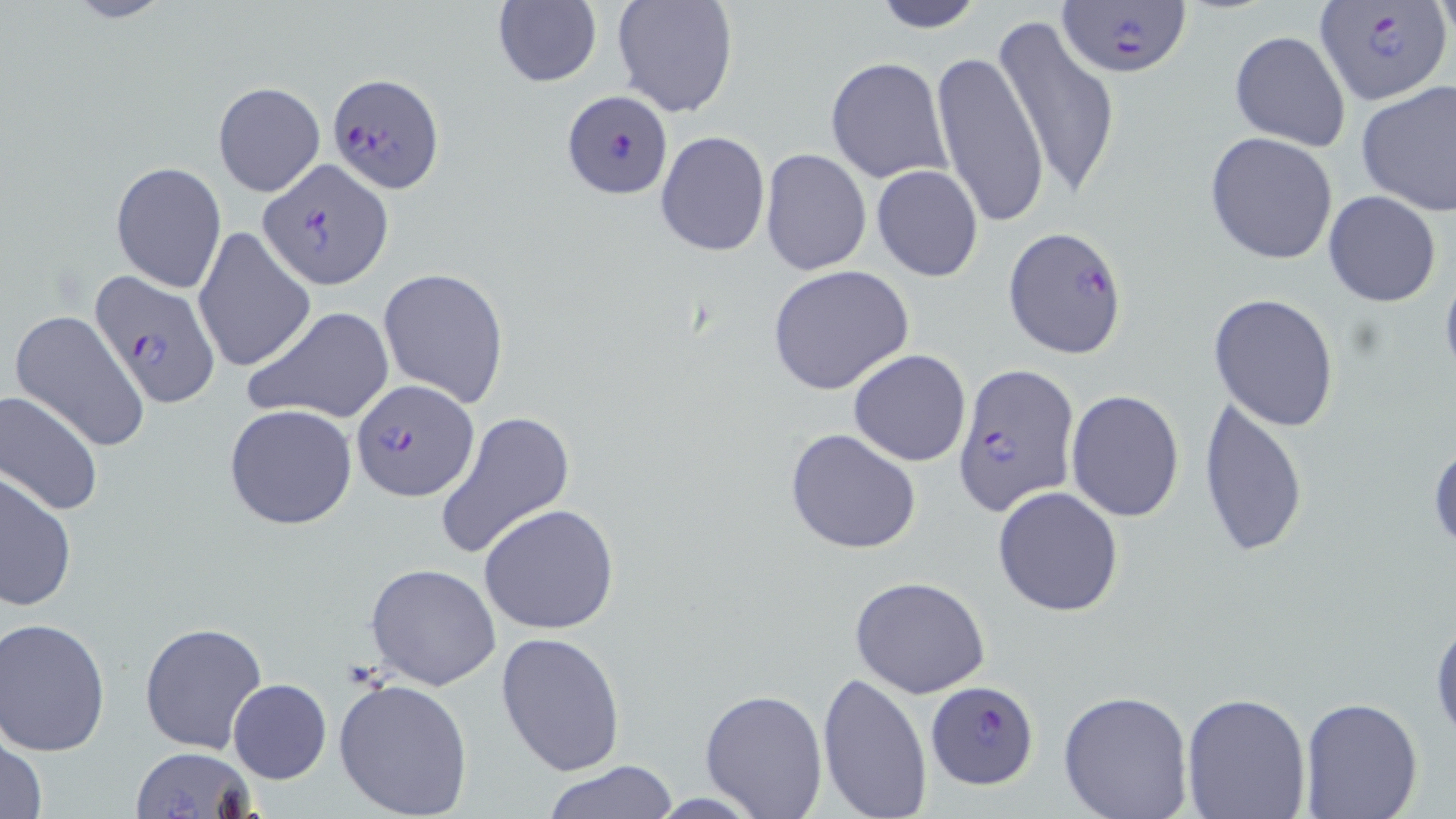

Summary:
  - Coordinate format: approximate bounding boxes as (x1, y1, x2, y2) in pixels
  - Plasmodium falciparum-infected red blood cell locations: (1056, 0, 1194, 80), (1314, 0, 1455, 107), (326, 72, 447, 195), (562, 89, 673, 200), (257, 159, 393, 290), (1004, 227, 1129, 357), (87, 272, 221, 408), (953, 360, 1080, 516), (350, 379, 478, 501), (927, 679, 1039, 788)
  - Uninfected red blood cell locations: (59, 0, 176, 24), (611, 0, 739, 119), (868, 0, 987, 32), (491, 1, 602, 89), (990, 17, 1123, 204), (1228, 29, 1351, 150), (930, 49, 1051, 229), (826, 56, 951, 183), (1355, 80, 1456, 218), (212, 82, 325, 196), (656, 130, 770, 256), (1205, 131, 1338, 265), (758, 149, 871, 277), (110, 161, 226, 292), (870, 165, 983, 281), (1324, 191, 1442, 307), (191, 226, 317, 374), (1439, 262, 1456, 385), (767, 264, 916, 397), (377, 267, 511, 407), (1209, 293, 1340, 432), (243, 306, 393, 425), (8, 309, 151, 453), (847, 348, 971, 466), (1066, 389, 1184, 523), (0, 390, 104, 517), (1197, 393, 1309, 559), (224, 404, 359, 531), (434, 409, 577, 562), (785, 428, 922, 554), (1428, 435, 1456, 554), (0, 468, 76, 612), (991, 484, 1124, 617), (479, 503, 620, 634), (364, 563, 502, 690), (848, 575, 991, 698), (1429, 607, 1456, 742), (1, 618, 115, 759), (139, 621, 269, 756), (495, 631, 625, 775), (816, 669, 932, 818), (333, 677, 477, 819), (228, 679, 332, 784), (698, 688, 829, 818), (1057, 690, 1194, 819), (1180, 690, 1312, 818), (1298, 697, 1424, 818), (2, 732, 49, 819), (132, 747, 255, 819), (540, 761, 683, 817)
  - Slide-level diagnosis: Plasmodium falciparum
  - Field of view: single
  - Magnification: 1000x
  - Modality: light microscopy
  - Stain: May-Grünwald-Giemsa
  - Image size: 1456×819 pixels
  - Preparation: thin blood smear